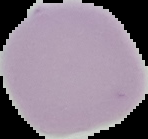
From a thin blood smear. Malaria status: uninfected. Image is 148×139 pixels. Cell region segmented out of the field of view; the surrounding area is masked to black.